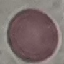
result = negative for malaria parasites
capture = smartphone camera at the microscope eyepiece
stain = Giemsa
image type = automatically extracted cell patch, resized to 64 × 64 pixels
preparation = thin blood film